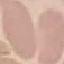
result = no malaria parasites detected
image type = cell patch, automatically extracted from a larger field of view and resized to 64 × 64 pixels
preparation = thin blood smear
capture = smartphone through the microscope eyepiece
stain = Giemsa